Locate every Plasmodium ovale-infected red blood cell.
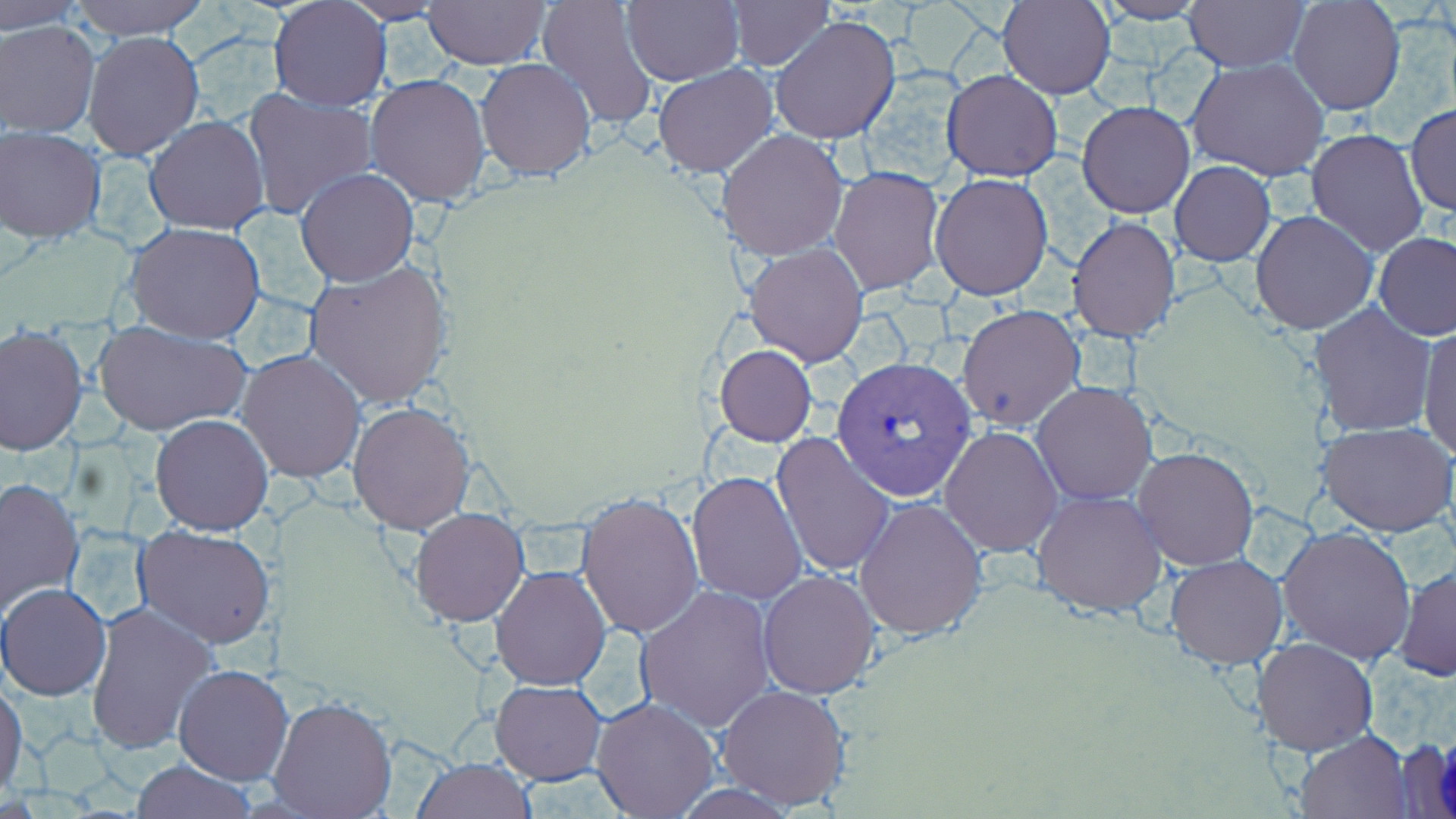

Approximate bounding boxes as named x1/y1/x2/y2 corners in pixels.
Plasmodium ovale-infected red blood cells: (x1=831, y1=356, x2=976, y2=503).

Summary:
  - Uninfected red blood cell locations: (x1=1, y1=0, x2=90, y2=32), (x1=65, y1=0, x2=211, y2=39), (x1=334, y1=0, x2=454, y2=25), (x1=537, y1=0, x2=658, y2=130), (x1=622, y1=0, x2=743, y2=85), (x1=723, y1=0, x2=835, y2=71), (x1=998, y1=0, x2=1114, y2=98), (x1=1184, y1=0, x2=1307, y2=72), (x1=1287, y1=0, x2=1405, y2=117), (x1=423, y1=1, x2=552, y2=70), (x1=1092, y1=1, x2=1211, y2=24), (x1=267, y1=2, x2=393, y2=112), (x1=771, y1=14, x2=900, y2=144), (x1=1, y1=21, x2=100, y2=137), (x1=81, y1=29, x2=205, y2=162), (x1=313, y1=50, x2=459, y2=198), (x1=477, y1=58, x2=597, y2=183), (x1=1186, y1=58, x2=1330, y2=181), (x1=652, y1=64, x2=779, y2=178), (x1=942, y1=69, x2=1063, y2=181), (x1=365, y1=75, x2=492, y2=207), (x1=241, y1=86, x2=376, y2=220), (x1=1078, y1=101, x2=1195, y2=218), (x1=1404, y1=105, x2=1455, y2=216), (x1=144, y1=115, x2=270, y2=235), (x1=1, y1=126, x2=106, y2=242), (x1=717, y1=128, x2=848, y2=261), (x1=1306, y1=128, x2=1428, y2=256), (x1=1170, y1=161, x2=1276, y2=266), (x1=830, y1=166, x2=944, y2=294), (x1=296, y1=169, x2=420, y2=286), (x1=930, y1=172, x2=1053, y2=300), (x1=1250, y1=210, x2=1378, y2=334), (x1=1067, y1=216, x2=1181, y2=340), (x1=124, y1=221, x2=267, y2=342), (x1=1374, y1=234, x2=1456, y2=341), (x1=744, y1=242, x2=869, y2=367), (x1=302, y1=260, x2=453, y2=409), (x1=1309, y1=303, x2=1437, y2=437), (x1=957, y1=305, x2=1084, y2=432), (x1=94, y1=320, x2=251, y2=438), (x1=1417, y1=323, x2=1456, y2=462), (x1=1, y1=325, x2=89, y2=454), (x1=715, y1=345, x2=817, y2=446), (x1=235, y1=349, x2=366, y2=483), (x1=1031, y1=380, x2=1157, y2=505), (x1=348, y1=403, x2=475, y2=534), (x1=150, y1=414, x2=274, y2=536), (x1=1318, y1=420, x2=1454, y2=537), (x1=938, y1=425, x2=1063, y2=557), (x1=772, y1=433, x2=897, y2=577), (x1=1132, y1=445, x2=1259, y2=571), (x1=687, y1=471, x2=808, y2=604), (x1=0, y1=475, x2=86, y2=615), (x1=1031, y1=489, x2=1169, y2=617), (x1=576, y1=492, x2=705, y2=638), (x1=855, y1=497, x2=988, y2=639), (x1=410, y1=508, x2=529, y2=627), (x1=1276, y1=524, x2=1420, y2=666), (x1=135, y1=526, x2=277, y2=647), (x1=1166, y1=554, x2=1287, y2=669), (x1=1394, y1=563, x2=1456, y2=684), (x1=491, y1=566, x2=612, y2=691), (x1=758, y1=569, x2=883, y2=698), (x1=1, y1=584, x2=110, y2=701), (x1=634, y1=584, x2=776, y2=731), (x1=83, y1=600, x2=217, y2=756), (x1=1254, y1=638, x2=1379, y2=755), (x1=173, y1=665, x2=292, y2=785), (x1=491, y1=680, x2=608, y2=785), (x1=0, y1=684, x2=27, y2=795), (x1=715, y1=684, x2=854, y2=811), (x1=266, y1=694, x2=397, y2=819), (x1=591, y1=697, x2=718, y2=818), (x1=1295, y1=729, x2=1415, y2=817), (x1=411, y1=756, x2=537, y2=819), (x1=130, y1=759, x2=258, y2=817)
  - Slide-level diagnosis: Plasmodium ovale
  - Modality: optical microscopy
  - Preparation: thin blood smear
  - Image size: 1456×819 pixels
  - Stain: May-Grünwald-Giemsa
  - Field of view: one of a larger specimen
  - Magnification: 1000x